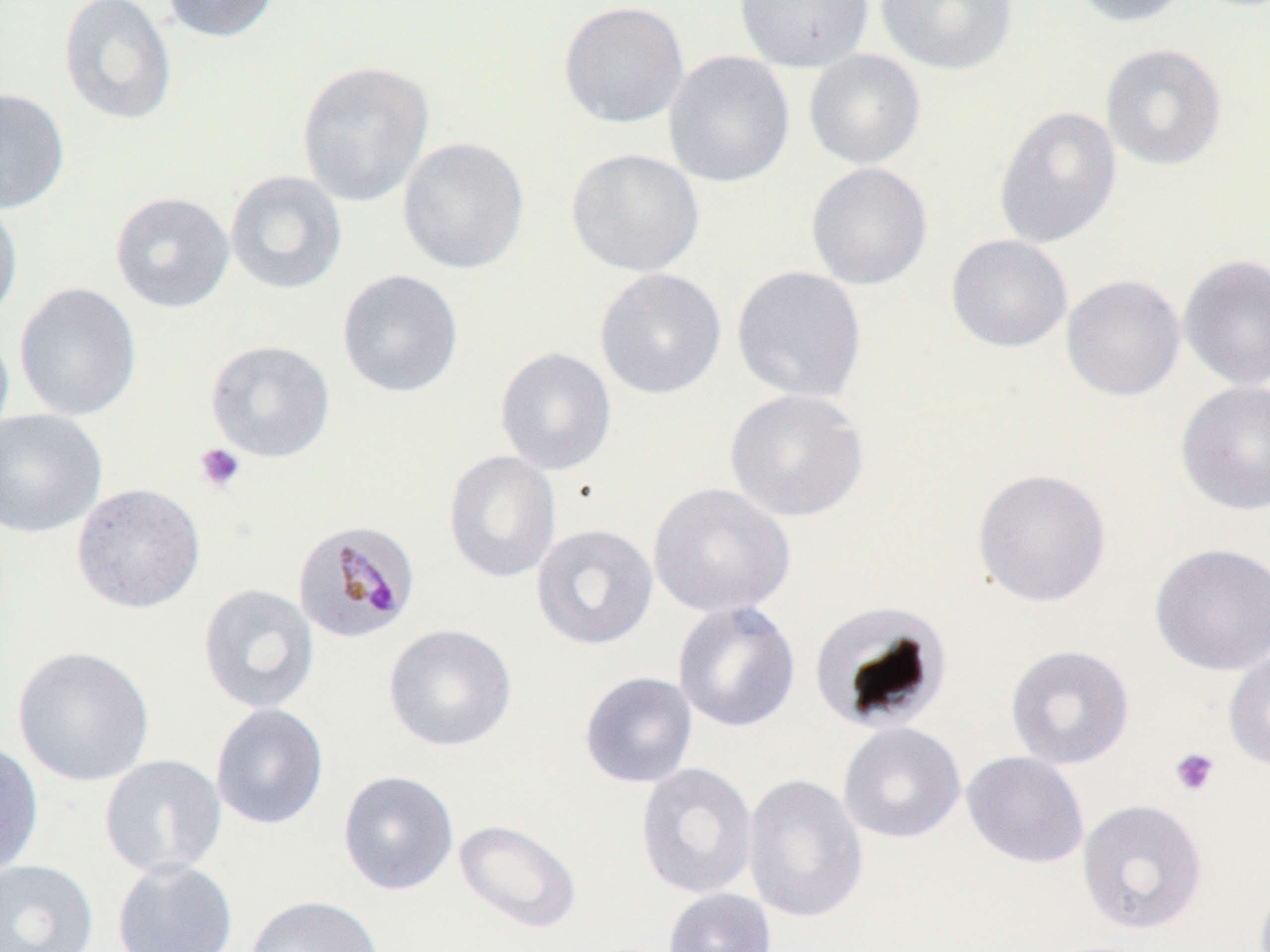

slide-level diagnosis = Plasmodium malariae
field of view = single
stain = May-Grünwald-Giemsa
magnification = 1000x
Plasmodium malariae-infected red blood cell locations = approximate bounding boxes as (x1,y1)-(x2,y2) corner pairs in pixels: (292,518)-(421,645)
uninfected red blood cell locations = approximate bounding boxes as (x1,y1)-(x2,y2) corner pairs in pixels: (58,0)-(177,126), (161,0)-(279,43), (734,0)-(874,72), (876,0)-(1018,75), (1070,0)-(1191,26), (559,1)-(689,128), (1100,43)-(1227,170), (804,49)-(926,170), (663,50)-(795,187), (296,60)-(434,207), (0,87)-(70,215), (994,105)-(1122,249), (398,137)-(530,274), (566,148)-(705,277), (806,162)-(933,290), (225,170)-(347,295), (111,192)-(234,312), (0,198)-(23,325), (946,234)-(1073,352), (1178,254)-(1270,391), (731,265)-(867,403), (595,267)-(727,400), (337,269)-(464,398), (1061,274)-(1186,401), (14,282)-(142,421), (0,324)-(15,448), (206,339)-(335,463), (494,346)-(617,475), (1175,380)-(1270,516), (724,388)-(869,522), (0,408)-(107,538), (443,450)-(562,583), (972,467)-(1111,607), (71,483)-(206,614), (647,483)-(795,618), (531,523)-(658,651), (1150,542)-(1270,675), (198,583)-(319,714), (672,600)-(801,733), (809,600)-(952,734), (383,623)-(517,751), (1005,644)-(1135,769), (12,645)-(155,787), (1223,650)-(1270,772), (579,671)-(698,788), (210,703)-(329,830), (838,721)-(966,844), (0,740)-(44,879), (961,751)-(1089,869), (99,754)-(227,878), (635,761)-(758,900), (337,770)-(459,896), (743,772)-(869,924), (1077,798)-(1207,935), (453,819)-(582,934), (112,858)-(238,952), (0,859)-(98,952), (663,888)-(776,952), (245,894)-(386,952)
image size = 1270×952 pixels
modality = light microscopy
preparation = thin blood film
platelet locations = approximate bounding boxes as (x1,y1)-(x2,y2) corner pairs in pixels: (195,443)-(245,493), (1169,748)-(1220,797)